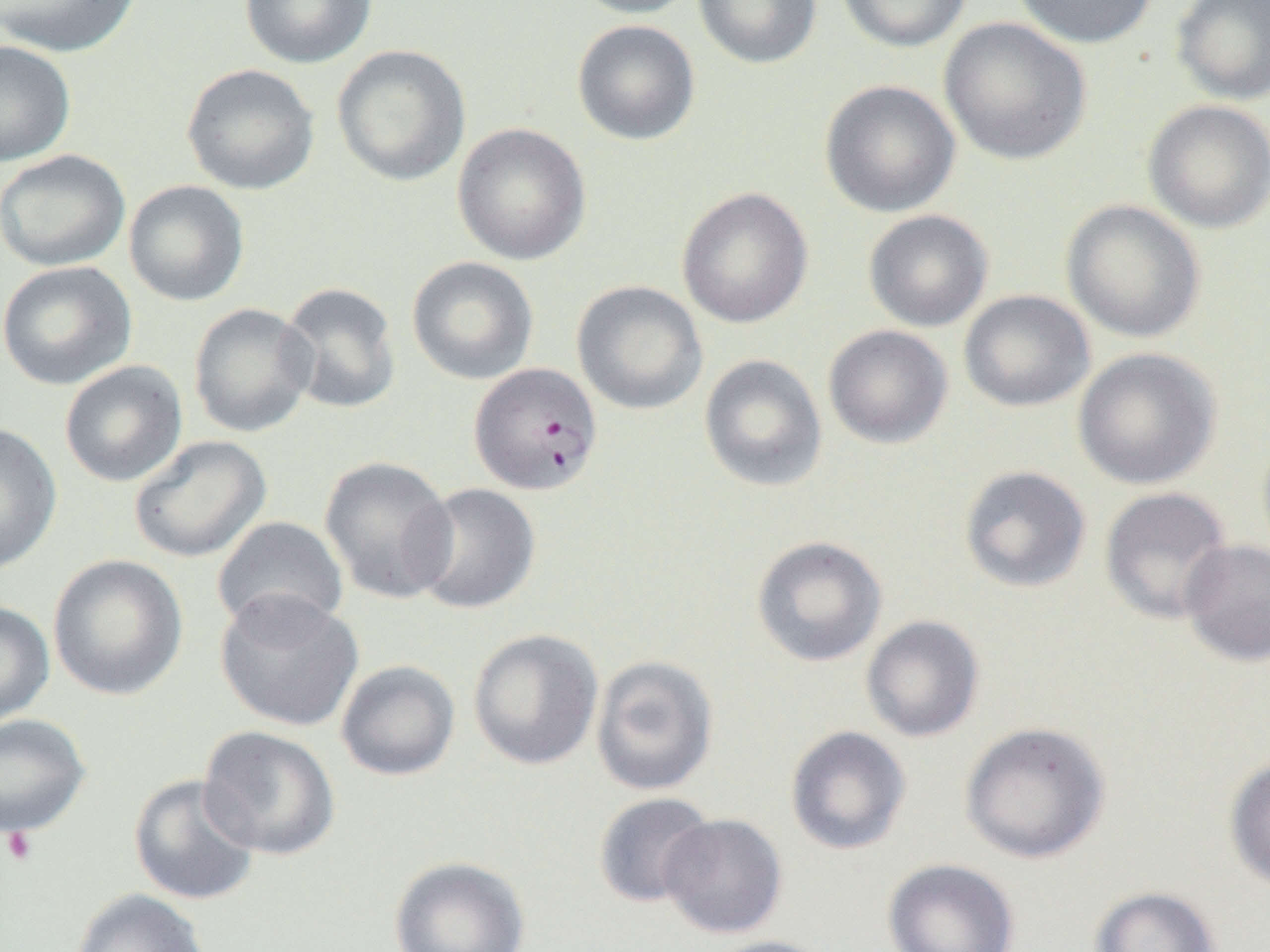

Approximate bounding boxes as (x1,y1)-(x2,y2) corner pairs in pixels. Plasmodium falciparum-infected red blood cell locations: (468,362)-(603,495). Uninfected red blood cell locations: (1,0)-(142,58), (239,0)-(377,69), (570,0)-(703,19), (693,0)-(823,69), (836,0)-(972,53), (1011,0)-(1158,49), (1170,0)-(1270,105), (939,17)-(1092,165), (572,19)-(700,146), (0,40)-(76,167), (331,44)-(471,186), (181,63)-(320,195), (819,79)-(961,218), (1142,99)-(1270,234), (451,122)-(591,265), (0,149)-(131,272), (123,180)-(250,306), (676,187)-(813,329), (1061,199)-(1206,344), (863,210)-(994,332), (406,256)-(539,385), (0,261)-(138,391), (571,280)-(707,415), (278,282)-(402,415), (958,289)-(1095,412), (188,302)-(317,438), (823,324)-(953,449), (1072,347)-(1223,490), (699,354)-(828,492), (58,360)-(188,487), (0,422)-(63,575), (129,435)-(272,563), (319,455)-(458,604), (958,465)-(1092,594), (408,483)-(541,615), (1099,486)-(1234,625), (212,515)-(349,637), (750,535)-(888,667), (1178,538)-(1270,667), (47,554)-(189,701), (214,590)-(364,732), (0,601)-(55,726), (860,615)-(985,743), (467,628)-(604,771), (590,655)-(720,796), (336,660)-(461,781), (0,713)-(92,838), (959,720)-(1112,864), (198,725)-(340,860), (784,725)-(912,856), (1224,754)-(1270,892), (128,773)-(262,906), (592,791)-(718,908), (658,813)-(787,939), (388,856)-(531,952), (882,857)-(1020,952), (1089,885)-(1222,952), (70,888)-(210,952), (700,935)-(840,952). Platelet locations: (2,826)-(39,866). Slide-level diagnosis: Plasmodium falciparum. One field of a larger specimen. Thin blood smear. Captured at 1000x magnification. Image is 1270×952 pixels. Light microscopy.